Assess this cell for malaria.
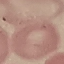

It is uninfected.

Summary:
  - Image type: automatically extracted cell patch, resized to 64 × 64 pixels
  - Stain: Giemsa
  - Capture: smartphone camera at the microscope eyepiece
  - Preparation: thin smear